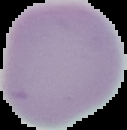

Image is 127×130 pixels. Malaria status: uninfected. The area outside the segmented cell region is set to black. From a thin blood smear.